Report the malaria status of this cell.
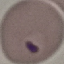
It is parasitized.

image type = automatically extracted cell patch, resized to 64 × 64 pixels
preparation = thin smear
stain = Giemsa
capture = smartphone camera at the microscope eyepiece